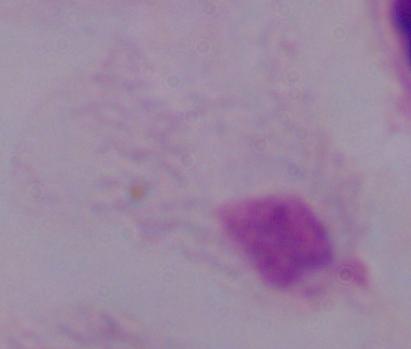
Summary:
  - Modality: micrograph
  - Identification: trichomonad
  - Magnification: 1000x